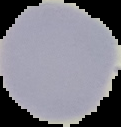
From a thin blood film. Image is 121×127 pixels. The area outside the segmented cell region is set to black. Malaria status: uninfected.